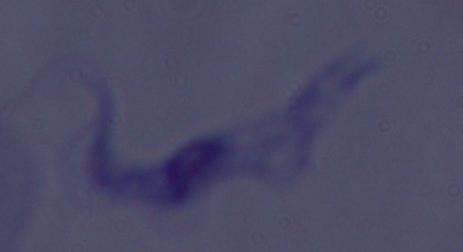
identification = trypanosome
modality = photomicrograph
magnification = 1000x